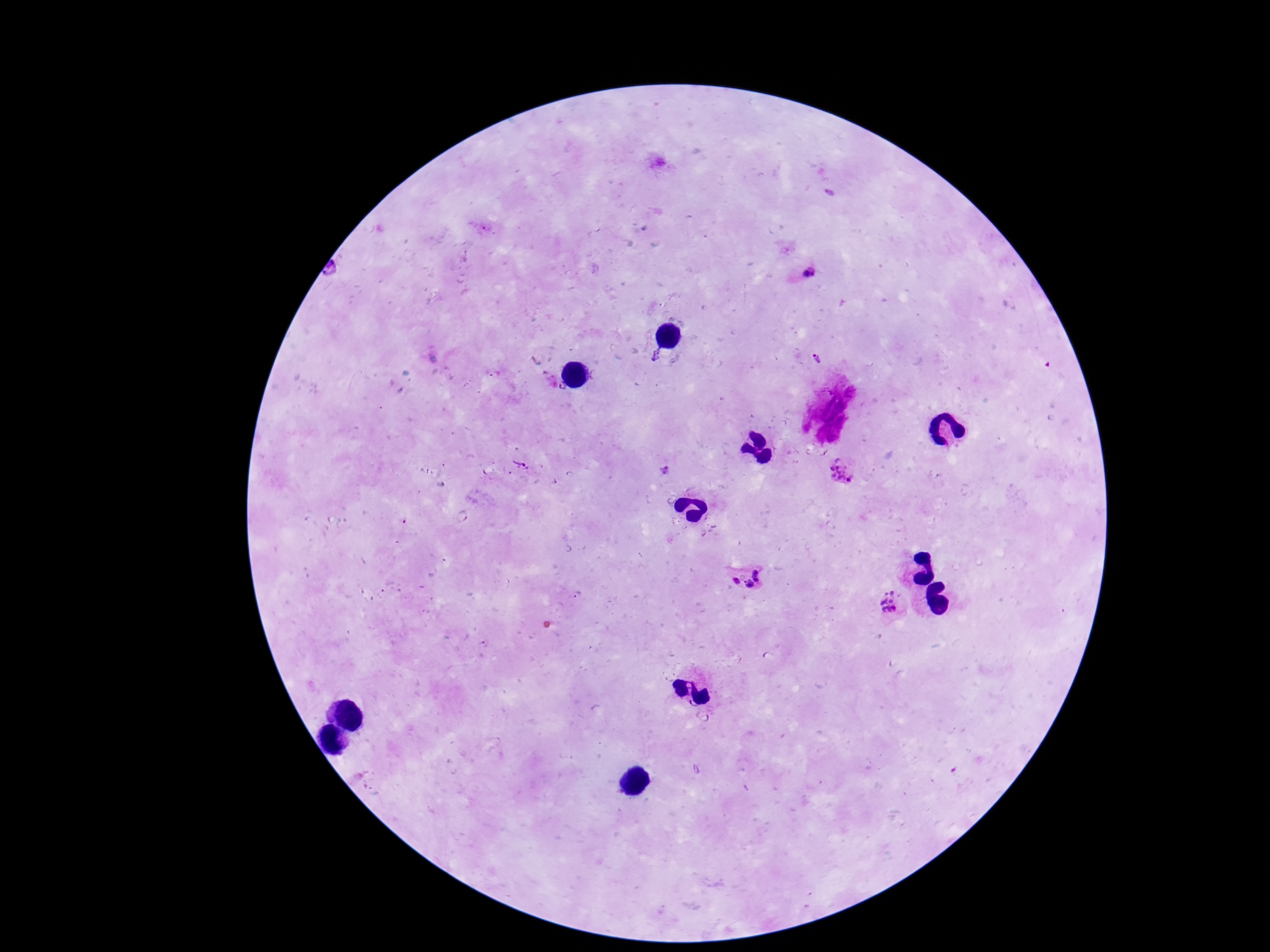
Approximate object centers, in pixels from the top-left corner.
Summary:
  - Plasmodium parasite locations: (x=830, y=194), (x=812, y=273), (x=655, y=358), (x=816, y=358), (x=562, y=389), (x=518, y=466), (x=663, y=470), (x=840, y=476), (x=744, y=578), (x=575, y=597), (x=891, y=604)
  - Image size: 1270×952 pixels
  - Magnification: 100x
  - Field of view: one from this slide
  - Capture: smartphone camera through the microscope eyepiece
  - Preparation: thick peripheral-blood smear
  - Stain: Giemsa
  - Patient malaria status: positive